Locate every Trypanosoma brucei.
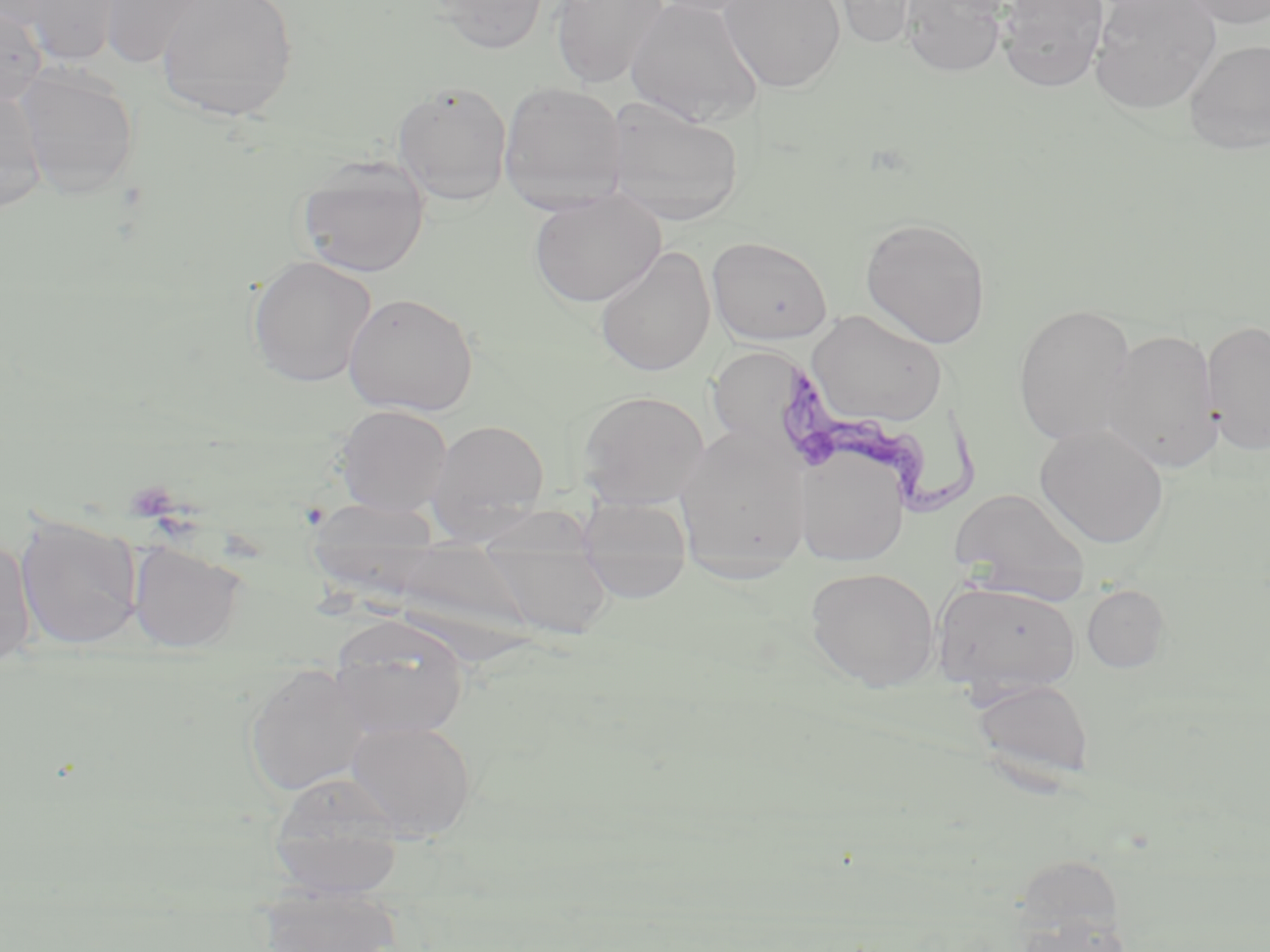
Approximate bounding boxes as (x1, y1, x2, y2) in pixels.
Trypanosoma brucei: (775, 361, 987, 514).

{
  "slide_level_diagnosis": "Trypanosoma brucei",
  "uninfected_red_blood_cell_locations": "approximate bounding boxes as (x1, y1, x2, y2) in pixels: (16, 0, 126, 65), (99, 0, 219, 67), (155, 0, 300, 122), (428, 0, 550, 55), (551, 0, 669, 88), (624, 0, 765, 128), (645, 0, 769, 17), (719, 0, 846, 93), (826, 0, 925, 50), (900, 0, 1007, 77), (997, 0, 1109, 92), (1090, 0, 1221, 114), (1180, 0, 1270, 29), (0, 4, 47, 106), (1183, 38, 1270, 154), (15, 64, 140, 200), (498, 80, 627, 212), (393, 82, 512, 206), (0, 88, 48, 212), (603, 95, 745, 226), (296, 155, 431, 278), (529, 191, 666, 308), (859, 217, 992, 348), (707, 235, 832, 345), (594, 246, 716, 377), (247, 255, 377, 388), (343, 292, 479, 416), (1013, 303, 1138, 446), (806, 311, 948, 429), (1201, 319, 1270, 456), (1101, 328, 1221, 473), (716, 345, 799, 439), (576, 390, 710, 508), (334, 404, 453, 516), (425, 418, 550, 539), (1035, 423, 1169, 550), (674, 427, 811, 574), (795, 449, 909, 566), (949, 486, 1091, 598), (577, 498, 692, 603), (305, 500, 444, 557), (15, 513, 144, 651), (480, 525, 614, 643), (0, 538, 36, 670), (128, 539, 247, 652), (806, 567, 941, 691), (931, 580, 1082, 701), (1082, 584, 1170, 673), (329, 615, 470, 740), (245, 662, 372, 797), (970, 676, 1095, 787), (345, 719, 478, 839), (268, 771, 407, 882), (256, 885, 403, 952), (1014, 908, 1133, 952)",
  "field_of_view": "single",
  "preparation": "thin blood film",
  "magnification": "1000x",
  "stain": "May-Grünwald-Giemsa",
  "image_size": "1270×952 pixels",
  "modality": "light microscopy"
}